Report the malaria status of this cell.
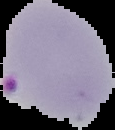

It is parasitized.

Summary:
  - Preparation: thin blood film
  - Image type: cell region segmented out of the field of view; surrounding area masked to black
  - Image size: 115×130 pixels